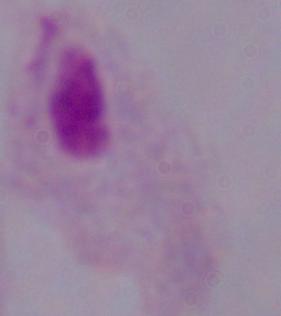

Summary:
  - Identification: trichomonad
  - Modality: photomicrograph
  - Magnification: 1000x